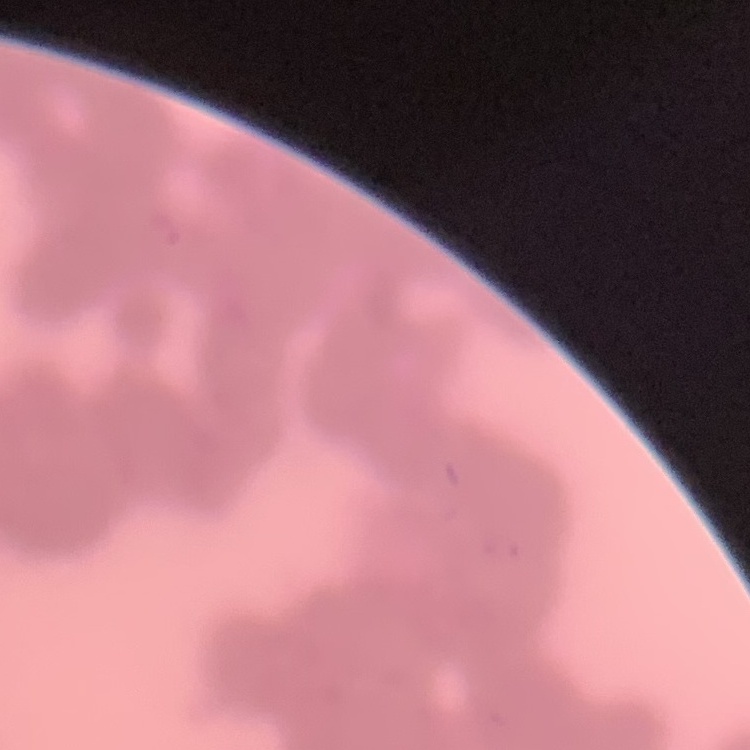

red blood cell morphology = rouleaux formation
preparation = thin blood smear
image type = one tile cut from a larger photomicrograph
stain = Field's or Giemsa